Assess this cell for malaria.
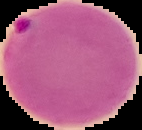
It is parasitized.

preparation = thin blood film
image type = cell region segmented out of the field of view; surrounding area masked to black
image size = 142×130 pixels